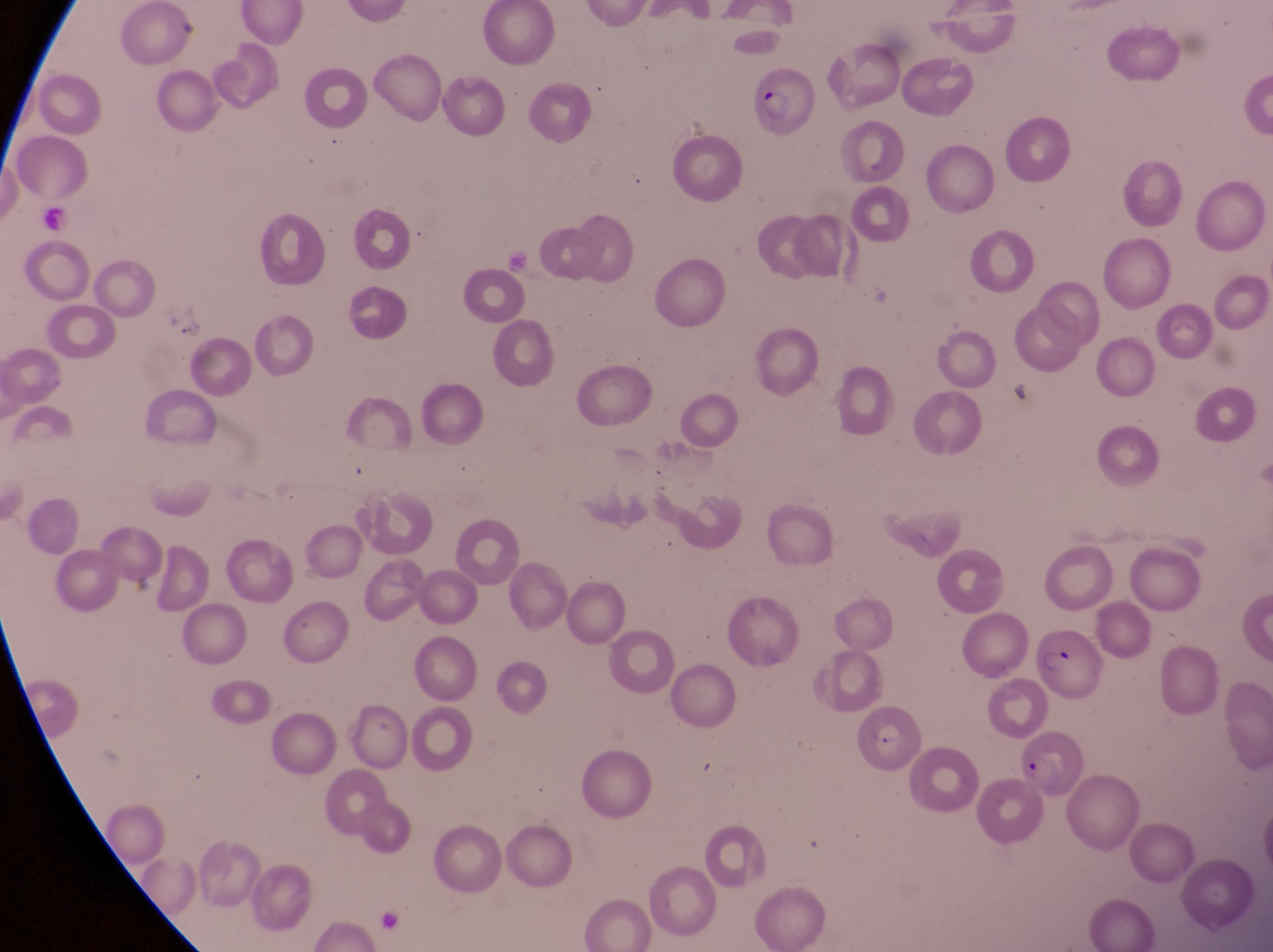

Approximate bounding boxes as [left, top, right, bottom] in pixels.
Summary:
  - Parasitised red blood cell locations: [743, 65, 815, 142], [1031, 629, 1106, 703], [1019, 729, 1088, 803]
  - Image size: 1273×952 pixels
  - Preparation: thin blood smear
  - Country: Uganda
  - Field of view: single
  - Capture: smartphone photograph through the eyepiece of an Olympus CX-23 microscope
  - Magnification: 1000x